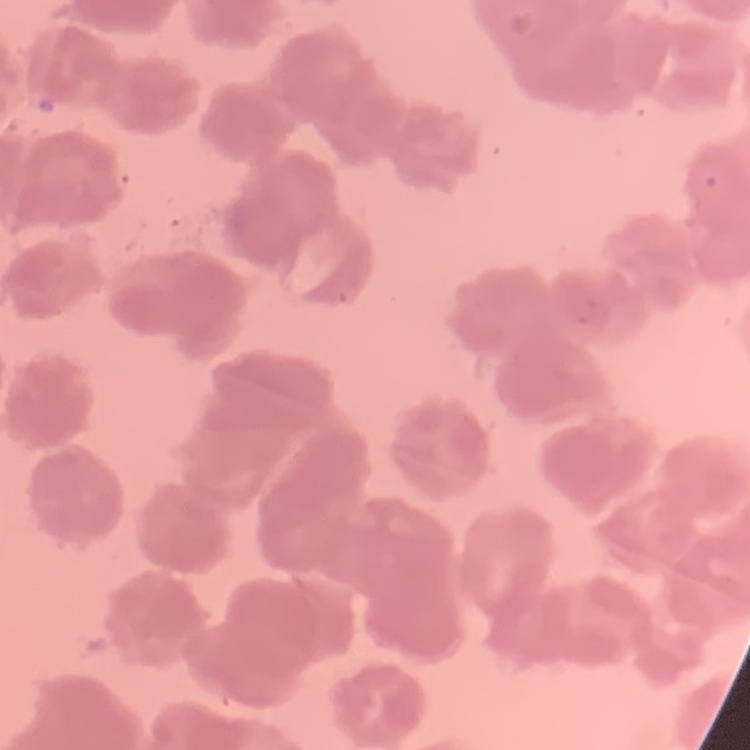
The erythrocytes exhibit rouleaux formation. Square crop of a larger photomicrograph. Field's or Giemsa stain. Thin peripheral smear.